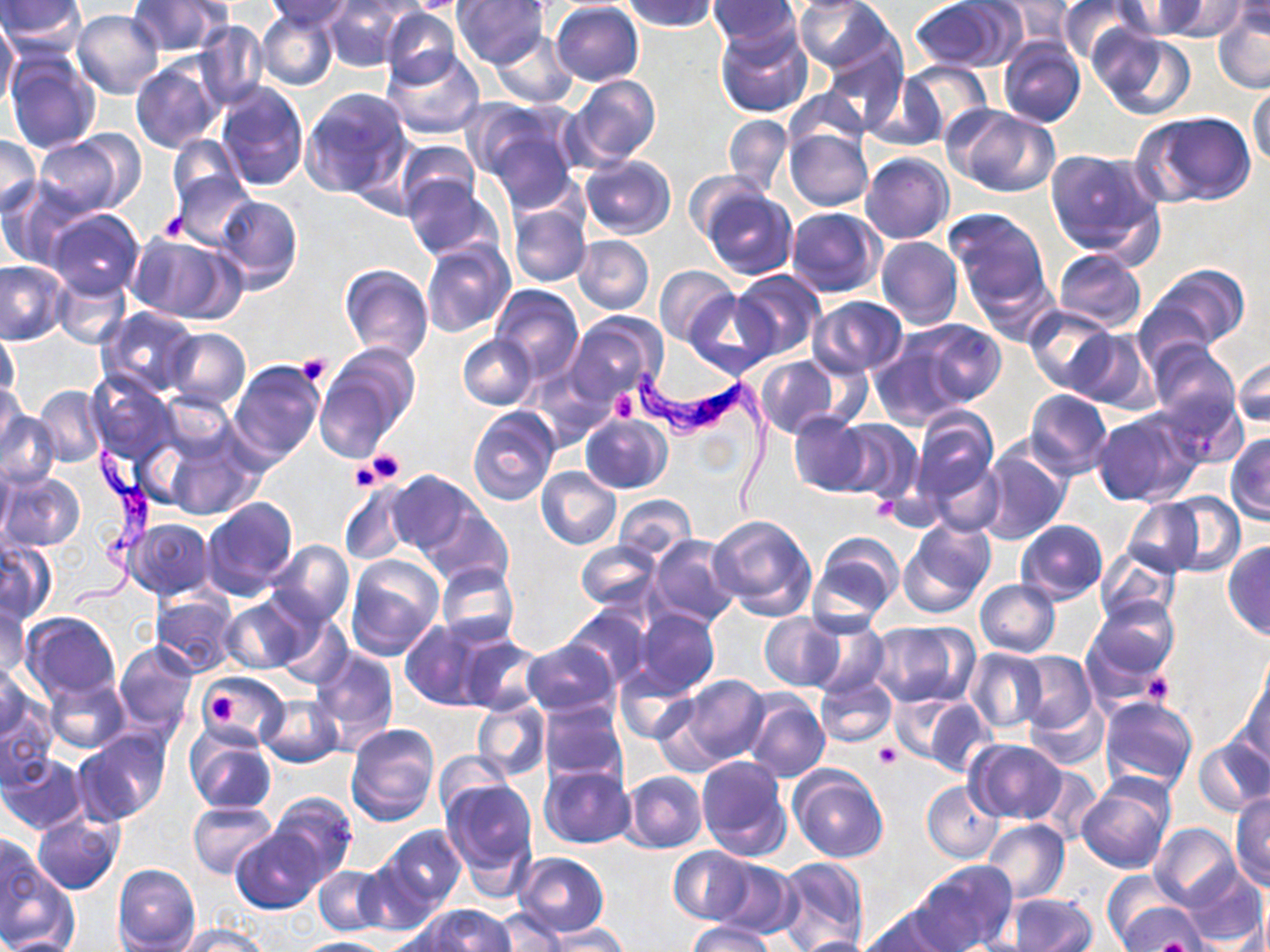

Summary:
  - Coordinate format: approximate bounding boxes as named x1/y1/x2/y2 corners in pixels
  - Trypanosoma brucei locations: (x1=631, y1=367, x2=775, y2=515), (x1=68, y1=448, x2=164, y2=616)
  - Uninfected red blood cell locations: (x1=0, y1=0, x2=87, y2=53), (x1=322, y1=0, x2=407, y2=71), (x1=403, y1=0, x2=477, y2=14), (x1=623, y1=0, x2=719, y2=33), (x1=708, y1=0, x2=800, y2=47), (x1=794, y1=0, x2=897, y2=76), (x1=909, y1=0, x2=1016, y2=73), (x1=982, y1=0, x2=1073, y2=49), (x1=1057, y1=0, x2=1144, y2=66), (x1=1112, y1=0, x2=1205, y2=40), (x1=1151, y1=0, x2=1252, y2=40), (x1=128, y1=1, x2=231, y2=56), (x1=263, y1=1, x2=355, y2=27), (x1=452, y1=1, x2=549, y2=69), (x1=550, y1=1, x2=644, y2=86), (x1=1227, y1=1, x2=1270, y2=37), (x1=1212, y1=6, x2=1270, y2=94), (x1=379, y1=7, x2=460, y2=88), (x1=258, y1=8, x2=338, y2=90), (x1=71, y1=9, x2=165, y2=98), (x1=0, y1=16, x2=19, y2=112), (x1=195, y1=21, x2=269, y2=110), (x1=714, y1=22, x2=813, y2=118), (x1=1092, y1=27, x2=1197, y2=122), (x1=490, y1=31, x2=579, y2=107), (x1=998, y1=38, x2=1086, y2=129), (x1=820, y1=40, x2=906, y2=134), (x1=382, y1=48, x2=486, y2=139), (x1=5, y1=52, x2=101, y2=154), (x1=132, y1=58, x2=224, y2=154), (x1=898, y1=61, x2=993, y2=142), (x1=565, y1=74, x2=660, y2=169), (x1=865, y1=75, x2=949, y2=152), (x1=215, y1=81, x2=308, y2=191), (x1=1248, y1=83, x2=1270, y2=169), (x1=300, y1=87, x2=412, y2=197), (x1=784, y1=87, x2=870, y2=154), (x1=948, y1=106, x2=1060, y2=199), (x1=478, y1=109, x2=583, y2=210), (x1=1132, y1=110, x2=1256, y2=207), (x1=724, y1=114, x2=793, y2=195), (x1=785, y1=128, x2=873, y2=210), (x1=33, y1=133, x2=135, y2=217), (x1=0, y1=134, x2=41, y2=218), (x1=167, y1=135, x2=246, y2=210), (x1=393, y1=138, x2=479, y2=214), (x1=1044, y1=147, x2=1164, y2=260), (x1=861, y1=152, x2=954, y2=244), (x1=579, y1=154, x2=676, y2=239), (x1=171, y1=169, x2=253, y2=249), (x1=685, y1=172, x2=765, y2=244), (x1=402, y1=176, x2=503, y2=262), (x1=0, y1=180, x2=89, y2=268), (x1=699, y1=184, x2=798, y2=280), (x1=214, y1=195, x2=302, y2=292), (x1=506, y1=203, x2=591, y2=288), (x1=784, y1=205, x2=885, y2=297), (x1=44, y1=208, x2=146, y2=299), (x1=944, y1=208, x2=1052, y2=316), (x1=126, y1=233, x2=237, y2=322), (x1=573, y1=236, x2=654, y2=314), (x1=876, y1=236, x2=963, y2=329), (x1=421, y1=239, x2=515, y2=341), (x1=1054, y1=249, x2=1145, y2=333), (x1=0, y1=260, x2=68, y2=345), (x1=338, y1=264, x2=434, y2=363), (x1=1146, y1=265, x2=1249, y2=354), (x1=655, y1=266, x2=739, y2=347), (x1=730, y1=269, x2=827, y2=360), (x1=52, y1=273, x2=131, y2=349), (x1=490, y1=285, x2=584, y2=383), (x1=685, y1=291, x2=774, y2=378), (x1=807, y1=296, x2=910, y2=378), (x1=1024, y1=306, x2=1118, y2=393), (x1=98, y1=307, x2=198, y2=397), (x1=565, y1=314, x2=664, y2=409), (x1=905, y1=318, x2=1006, y2=410), (x1=165, y1=327, x2=249, y2=410), (x1=0, y1=328, x2=20, y2=407), (x1=1065, y1=328, x2=1158, y2=413), (x1=458, y1=334, x2=537, y2=409), (x1=867, y1=336, x2=971, y2=431), (x1=1146, y1=340, x2=1241, y2=436), (x1=316, y1=344, x2=419, y2=457), (x1=1232, y1=354, x2=1270, y2=430), (x1=754, y1=355, x2=840, y2=439), (x1=229, y1=360, x2=325, y2=468), (x1=87, y1=372, x2=176, y2=465), (x1=0, y1=381, x2=25, y2=457), (x1=34, y1=385, x2=106, y2=468), (x1=1024, y1=388, x2=1112, y2=478), (x1=160, y1=391, x2=238, y2=464), (x1=467, y1=406, x2=559, y2=507), (x1=910, y1=407, x2=1000, y2=515), (x1=0, y1=411, x2=60, y2=490), (x1=1091, y1=411, x2=1198, y2=506), (x1=789, y1=412, x2=873, y2=496), (x1=579, y1=414, x2=671, y2=494), (x1=833, y1=420, x2=922, y2=504), (x1=1226, y1=432, x2=1270, y2=524), (x1=162, y1=434, x2=261, y2=519), (x1=978, y1=445, x2=1069, y2=543), (x1=921, y1=450, x2=1007, y2=537), (x1=0, y1=455, x2=14, y2=545), (x1=536, y1=466, x2=622, y2=550), (x1=387, y1=470, x2=477, y2=556), (x1=1, y1=473, x2=85, y2=551), (x1=338, y1=479, x2=415, y2=566), (x1=613, y1=493, x2=695, y2=562), (x1=1156, y1=493, x2=1245, y2=576), (x1=200, y1=497, x2=298, y2=602), (x1=1122, y1=499, x2=1204, y2=575), (x1=422, y1=507, x2=512, y2=589), (x1=706, y1=511, x2=818, y2=619), (x1=128, y1=518, x2=215, y2=599), (x1=899, y1=520, x2=994, y2=621), (x1=1015, y1=520, x2=1106, y2=604), (x1=810, y1=533, x2=904, y2=626), (x1=646, y1=535, x2=740, y2=629), (x1=264, y1=541, x2=354, y2=629), (x1=576, y1=541, x2=661, y2=611), (x1=0, y1=542, x2=57, y2=624), (x1=1223, y1=542, x2=1270, y2=640), (x1=1094, y1=545, x2=1181, y2=626), (x1=346, y1=555, x2=444, y2=660), (x1=436, y1=564, x2=519, y2=647), (x1=425, y1=575, x2=524, y2=707), (x1=975, y1=579, x2=1061, y2=657), (x1=151, y1=591, x2=240, y2=677), (x1=218, y1=597, x2=309, y2=675), (x1=1084, y1=598, x2=1179, y2=690), (x1=0, y1=599, x2=29, y2=683), (x1=564, y1=607, x2=651, y2=690), (x1=629, y1=608, x2=719, y2=701), (x1=22, y1=612, x2=120, y2=700), (x1=273, y1=614, x2=353, y2=690), (x1=758, y1=615, x2=843, y2=690), (x1=801, y1=615, x2=889, y2=698), (x1=400, y1=618, x2=501, y2=710), (x1=869, y1=621, x2=980, y2=709), (x1=457, y1=636, x2=543, y2=714), (x1=113, y1=639, x2=197, y2=733), (x1=522, y1=639, x2=619, y2=719), (x1=310, y1=647, x2=399, y2=754), (x1=964, y1=648, x2=1048, y2=733), (x1=1011, y1=652, x2=1097, y2=735), (x1=0, y1=664, x2=35, y2=743), (x1=615, y1=664, x2=701, y2=743), (x1=1240, y1=670, x2=1270, y2=765), (x1=44, y1=672, x2=131, y2=754), (x1=199, y1=672, x2=286, y2=743), (x1=673, y1=674, x2=770, y2=766), (x1=815, y1=674, x2=896, y2=749), (x1=742, y1=692, x2=830, y2=782), (x1=257, y1=693, x2=344, y2=766), (x1=1099, y1=694, x2=1197, y2=791), (x1=914, y1=695, x2=995, y2=778), (x1=0, y1=696, x2=58, y2=790), (x1=1026, y1=697, x2=1107, y2=770), (x1=472, y1=698, x2=550, y2=782), (x1=538, y1=701, x2=628, y2=786), (x1=345, y1=722, x2=439, y2=826), (x1=186, y1=729, x2=275, y2=815), (x1=75, y1=730, x2=170, y2=826), (x1=1193, y1=736, x2=1270, y2=818), (x1=965, y1=740, x2=1068, y2=822), (x1=432, y1=751, x2=512, y2=817), (x1=1, y1=753, x2=89, y2=834), (x1=696, y1=756, x2=792, y2=861), (x1=537, y1=764, x2=635, y2=849), (x1=1033, y1=765, x2=1105, y2=843), (x1=789, y1=766, x2=887, y2=864), (x1=621, y1=770, x2=707, y2=853), (x1=1076, y1=775, x2=1176, y2=874), (x1=440, y1=778, x2=539, y2=878), (x1=922, y1=781, x2=1004, y2=863), (x1=1230, y1=791, x2=1270, y2=888), (x1=268, y1=792, x2=358, y2=885), (x1=187, y1=800, x2=278, y2=879), (x1=32, y1=812, x2=123, y2=894), (x1=981, y1=819, x2=1069, y2=904), (x1=1150, y1=821, x2=1241, y2=910), (x1=379, y1=825, x2=466, y2=913), (x1=232, y1=827, x2=325, y2=912), (x1=0, y1=830, x2=46, y2=924), (x1=669, y1=845, x2=755, y2=924), (x1=514, y1=852, x2=609, y2=936), (x1=356, y1=856, x2=443, y2=937), (x1=775, y1=857, x2=868, y2=952), (x1=0, y1=858, x2=77, y2=949), (x1=709, y1=858, x2=798, y2=939), (x1=916, y1=860, x2=1017, y2=951), (x1=113, y1=864, x2=200, y2=951), (x1=313, y1=865, x2=387, y2=936), (x1=1181, y1=867, x2=1267, y2=946), (x1=1101, y1=869, x2=1187, y2=945), (x1=1003, y1=893, x2=1097, y2=952), (x1=1114, y1=902, x2=1209, y2=951), (x1=419, y1=904, x2=516, y2=951), (x1=859, y1=905, x2=963, y2=952), (x1=486, y1=907, x2=568, y2=951), (x1=688, y1=922, x2=777, y2=951), (x1=174, y1=923, x2=270, y2=952), (x1=539, y1=926, x2=631, y2=951), (x1=2, y1=934, x2=82, y2=952), (x1=784, y1=935, x2=882, y2=952), (x1=290, y1=937, x2=390, y2=952)
  - Platelet locations: (x1=156, y1=211, x2=188, y2=242), (x1=296, y1=352, x2=332, y2=385), (x1=610, y1=392, x2=638, y2=422), (x1=361, y1=450, x2=406, y2=488), (x1=1142, y1=669, x2=1175, y2=706), (x1=204, y1=684, x2=247, y2=727), (x1=873, y1=743, x2=901, y2=769)
  - Slide-level diagnosis: Trypanosoma brucei
  - Modality: light microscopy
  - Stain: May-Grünwald-Giemsa
  - Image size: 1270×952 pixels
  - Preparation: thin blood film
  - Field of view: one of a larger specimen
  - Magnification: 1000x